Report the malaria status of this cell.
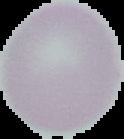

It is uninfected.

image size = 124×139 pixels
image type = segmented cell region with the area outside set to black
preparation = thin blood film